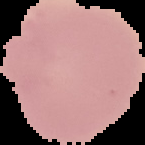

Summary:
  - Image type: segmented cell region on a black background
  - Result: no Plasmodium parasites detected
  - Image size: 145×145 pixels
  - Preparation: thin blood film